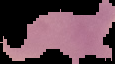

image size = 115×64 pixels
preparation = thin blood film
image type = cell region segmented out of the field of view; surrounding area masked to black
result = no Plasmodium parasites seen